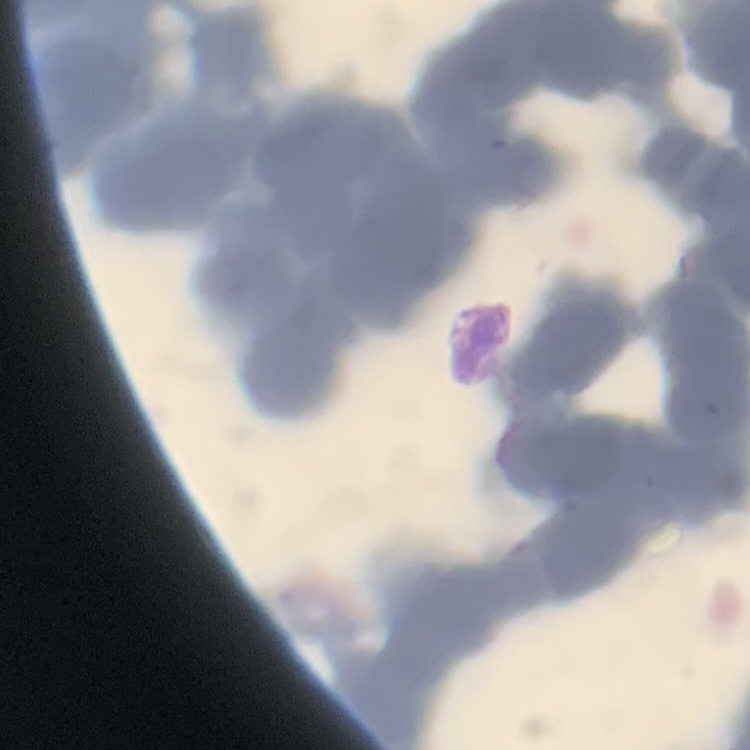

{
  "erythrocyte_morphology": "rouleaux formation",
  "stain": "Field's or Giemsa",
  "image_type": "square crop of a larger photomicrograph",
  "preparation": "thin blood smear"
}